Classify this cell by malaria status.
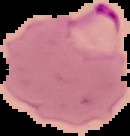
It is parasitized.

image type = segmented cell region on a black background
image size = 130×136 pixels
preparation = thin blood film